Point out leukocytes.
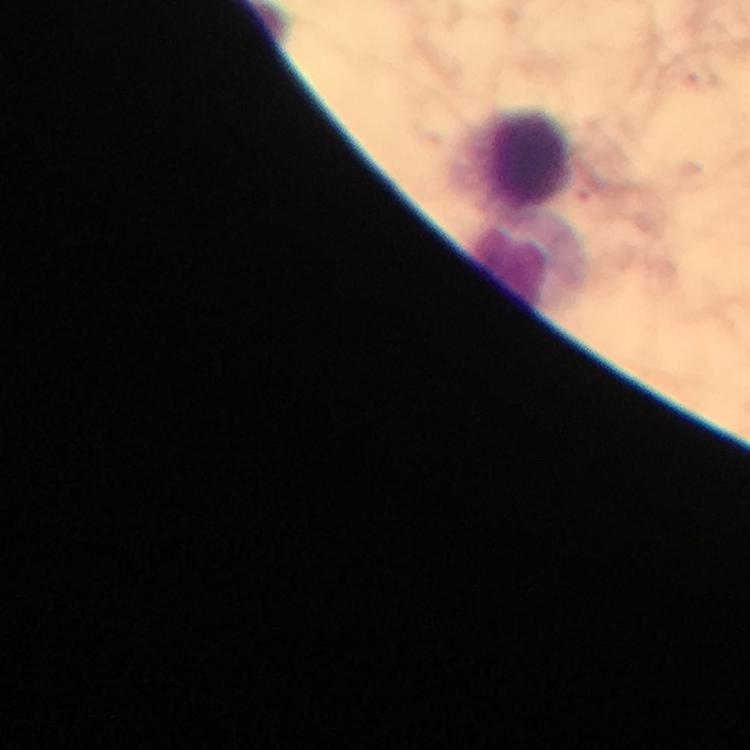

Approximate centers as [x, y] in pixels.
Leukocytes: [523, 159], [529, 261].

context: from a diagnostic examination for malaria
cropped_from: a single field of view
immersion_oil: applied
malaria_parasites: none detected
image_size: 750×750 pixels
stain: Giemsa
capture: smartphone mounted on the microscope
magnification: 100x
preparation: thick blood smear